Look for Plasmodium parasites.
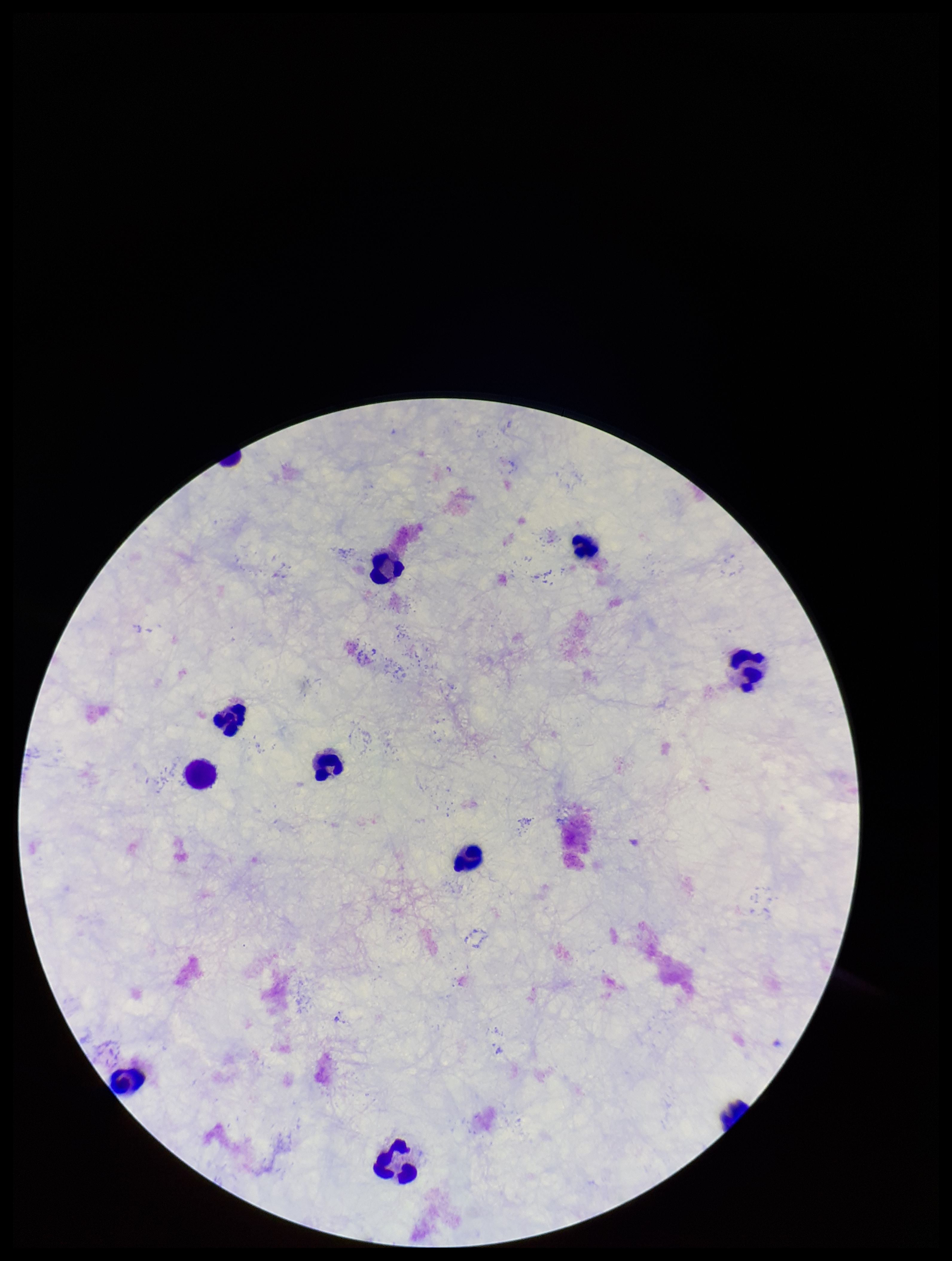
None detected.

Preparation: thick smear. Leukocyte count: 10. Stained with Giemsa. Parasite count: 0. One field from this slide. Image is 952×1261 pixels. Smartphone photograph taken through the eyepiece of a microscope. Patient malaria status: negative.